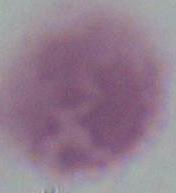

A red blood cell is shown. Captured at 1000x magnification. Micrograph.